Give the extent of all uninfected red blood cells.
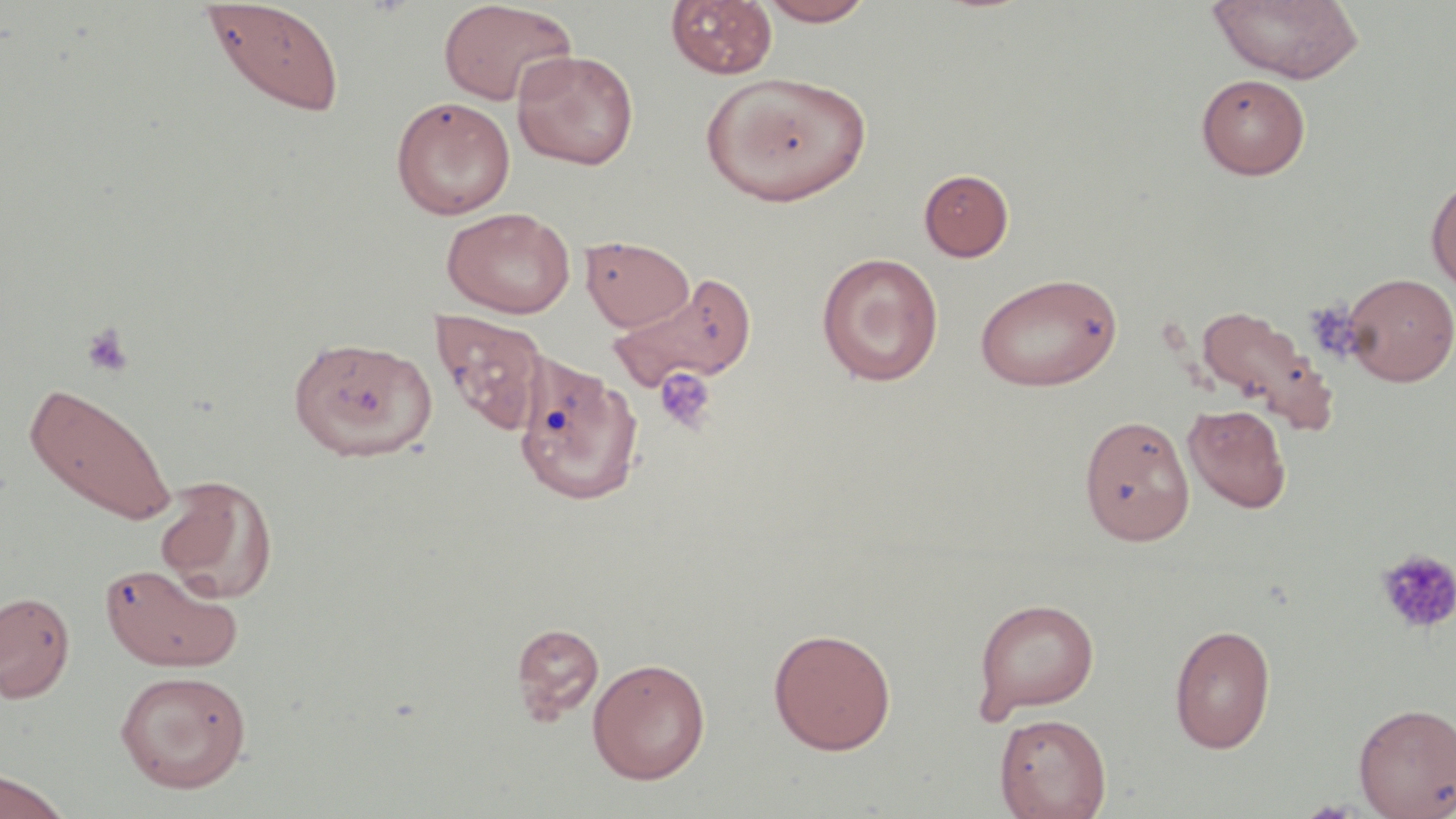
Approximate bounding boxes as (x1, y1, x2, y2) in pixels.
Uninfected red blood cells: (758, 0, 877, 26), (1207, 0, 1365, 84), (199, 1, 345, 118), (437, 1, 577, 107), (666, 1, 777, 79), (512, 50, 639, 171), (704, 72, 872, 206), (1196, 73, 1310, 180), (390, 96, 515, 219), (918, 169, 1014, 261), (1427, 177, 1456, 293), (441, 206, 575, 319), (580, 235, 697, 332), (816, 253, 944, 387), (609, 272, 758, 391), (974, 272, 1123, 392), (1341, 272, 1456, 386), (1194, 303, 1335, 431), (430, 310, 548, 437), (288, 336, 435, 462), (513, 356, 644, 507), (24, 379, 178, 526), (1182, 403, 1292, 514), (1077, 412, 1193, 542), (153, 475, 277, 602), (101, 557, 247, 672), (0, 590, 76, 703), (973, 597, 1099, 720), (511, 621, 605, 724), (1169, 623, 1276, 753), (768, 627, 897, 755), (587, 657, 711, 784), (115, 669, 251, 793), (1354, 701, 1456, 818), (994, 712, 1111, 819), (0, 768, 73, 818).

Platelet locations: (1303, 300, 1366, 363), (82, 322, 135, 377), (653, 367, 717, 433), (1375, 548, 1456, 634). Slide-level diagnosis: negative for blood parasites. Image is 1456×819 pixels. 1000x magnification. One field of a larger specimen. Light microscopy. May-Grünwald-Giemsa-stained preparation. Thin blood film.